Assess this cell for malaria.
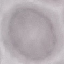
Uninfected.

Summary:
  - Stain: Giemsa
  - Image type: cell patch, automatically extracted from a larger field of view and resized to 64 × 64 pixels
  - Capture: smartphone camera at the microscope eyepiece
  - Preparation: thin blood film